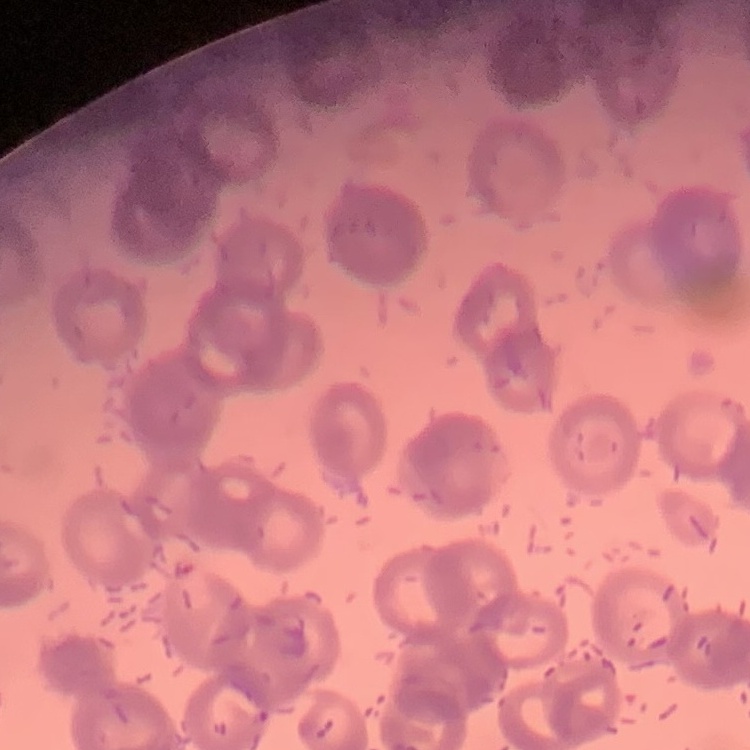
erythrocyte morphology = rouleaux formation
stain = Field's or Giemsa
image type = one tile cut from a larger photomicrograph
preparation = thin blood film